Point out each leukocyte.
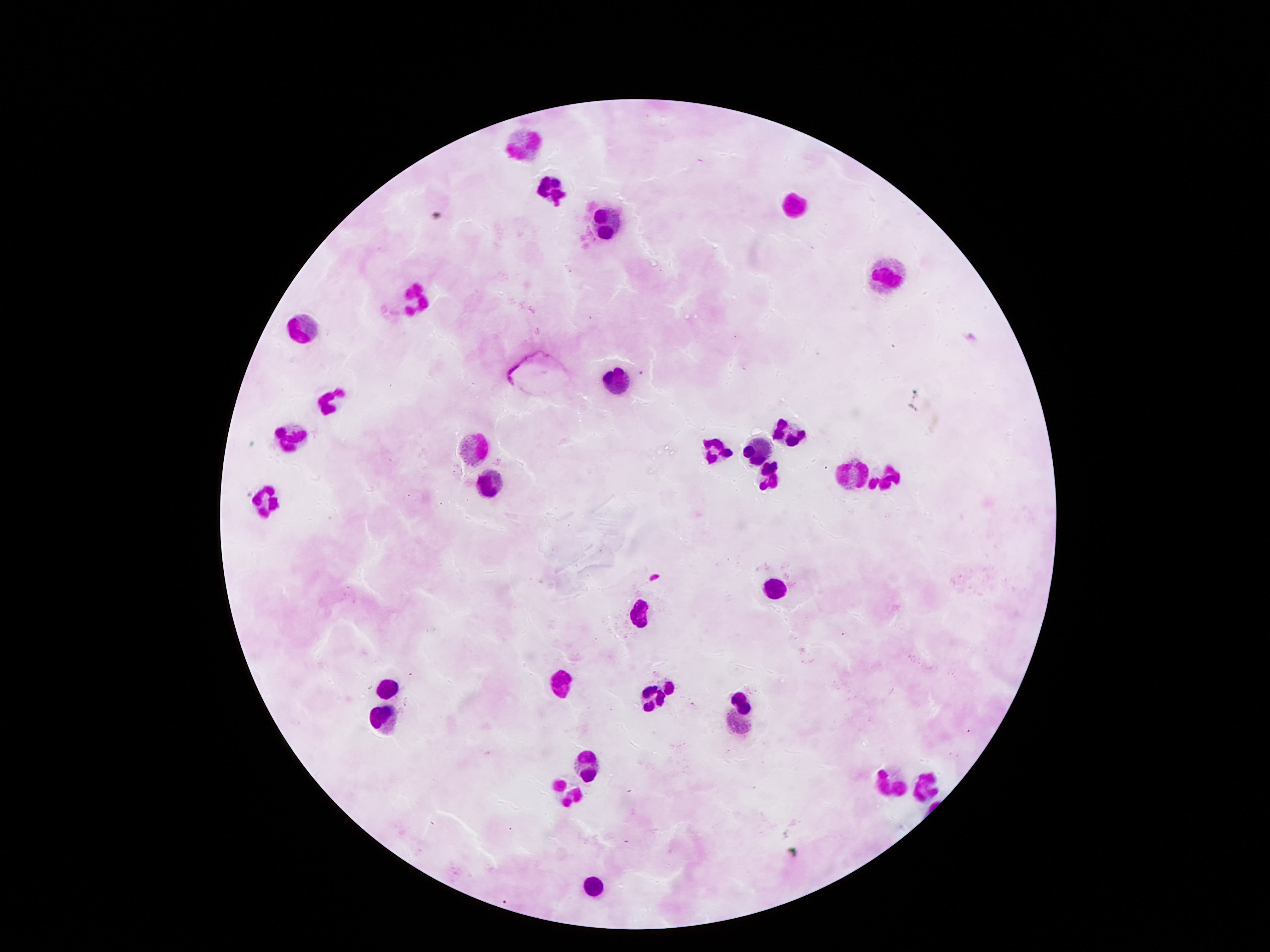

Approximate centers as [x, y] in pixels.
Leukocytes: [520, 141], [552, 187], [793, 201], [603, 225], [888, 278], [417, 293], [305, 324], [617, 382], [326, 400], [786, 432], [295, 433], [720, 445], [756, 445], [472, 447], [767, 472], [850, 473], [493, 478], [882, 479], [266, 497], [772, 590], [640, 612], [558, 684], [668, 689], [393, 692], [657, 702], [741, 702], [385, 723], [587, 760], [927, 780], [886, 784], [564, 792], [595, 889].

{
  "preparation": "thick blood film",
  "stain": "Giemsa",
  "magnification": "100x",
  "patient_malaria_status": "negative",
  "field_of_view": "single",
  "capture": "smartphone camera through the microscope eyepiece",
  "image_size": "1270×952 pixels"
}